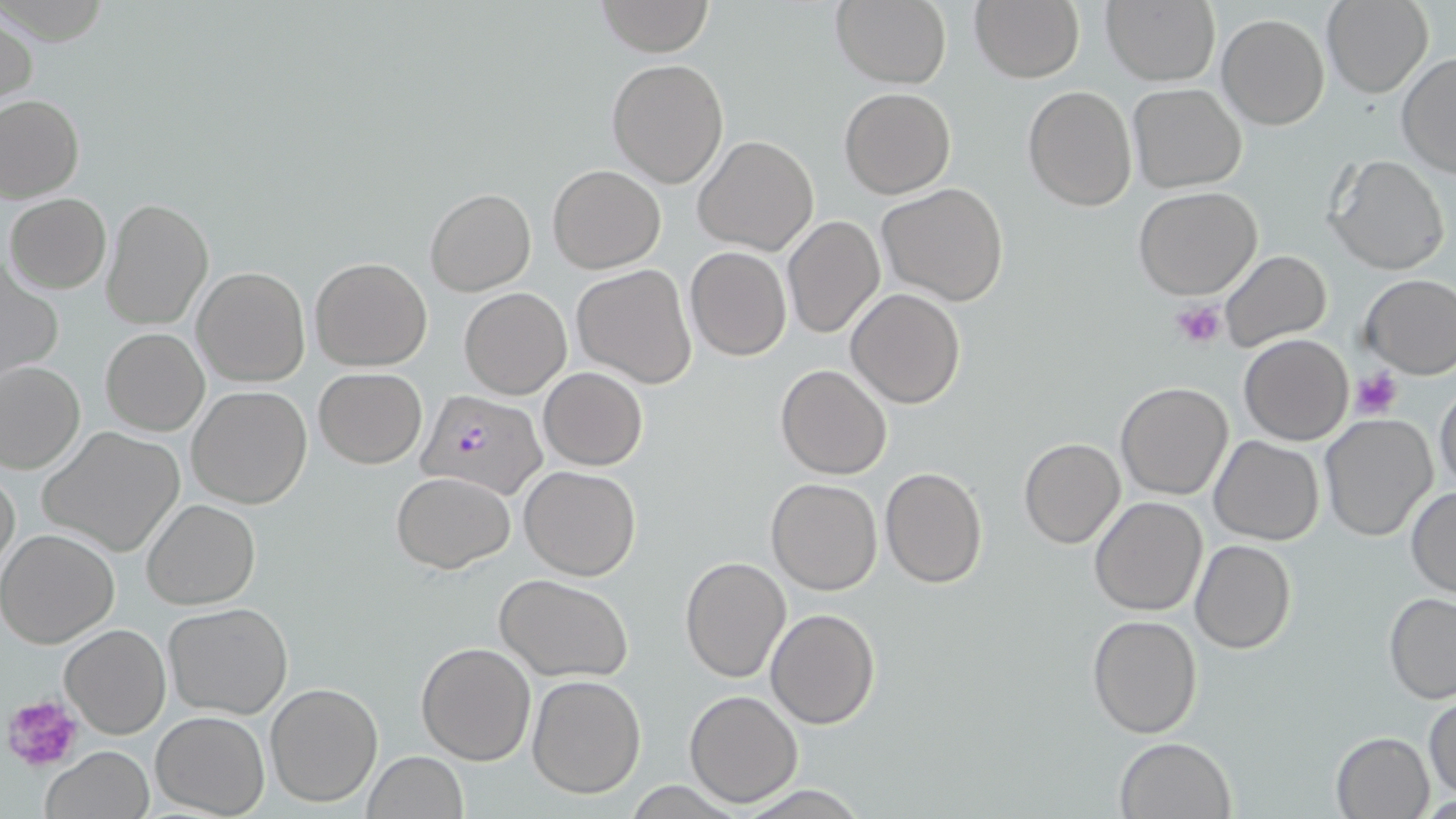

slide_level_diagnosis: Plasmodium falciparum
platelet_locations: 'approximate bounding boxes as [x1, y1, x2, y2] in pixels: [1172, 299, 1226, 351], [1349, 369, 1404, 420], [5, 694, 85, 770]'
stain: May-Grünwald-Giemsa
image_size: 1456×819 pixels
modality: light microscopy
preparation: thin blood smear
plasmodium_falciparum_infected_red_blood_cell_locations: 'approximate bounding boxes as [x1, y1, x2, y2] in pixels: [418, 390, 548, 501]'
field_of_view: one of a larger specimen
magnification: 1000x
uninfected_red_blood_cell_locations: 'approximate bounding boxes as [x1, y1, x2, y2] in pixels: [971, 0, 1085, 85], [1101, 0, 1219, 88], [596, 1, 714, 56], [830, 1, 951, 88], [1322, 1, 1432, 97], [1, 9, 37, 113], [1215, 13, 1329, 130], [1396, 53, 1456, 179], [605, 58, 729, 189], [1128, 84, 1247, 193], [1022, 85, 1137, 212], [839, 87, 956, 199], [0, 94, 84, 202], [693, 135, 820, 256], [1325, 153, 1450, 276], [548, 164, 665, 273], [876, 182, 1010, 306], [1132, 186, 1262, 300], [425, 189, 536, 296], [5, 193, 111, 294], [100, 198, 214, 331], [781, 215, 885, 339], [684, 247, 792, 362], [1218, 249, 1331, 352], [309, 256, 433, 370], [1, 261, 64, 383], [573, 264, 696, 389], [192, 265, 309, 387], [1360, 274, 1456, 379], [459, 286, 572, 399], [846, 288, 965, 409], [100, 327, 209, 436], [1239, 334, 1353, 446], [1, 361, 85, 473], [775, 365, 892, 480], [313, 367, 427, 468], [539, 367, 648, 471], [1434, 378, 1456, 496], [1115, 381, 1234, 500], [186, 385, 313, 510], [1318, 413, 1439, 543], [37, 425, 187, 557], [1210, 435, 1324, 544], [1018, 437, 1126, 549], [1, 461, 20, 579], [519, 465, 642, 581], [879, 466, 988, 587], [392, 471, 515, 573], [766, 477, 882, 596], [1405, 485, 1456, 598], [1088, 496, 1208, 616], [142, 499, 260, 610], [0, 528, 119, 648], [1190, 540, 1296, 655], [680, 557, 790, 682], [495, 574, 633, 681], [1383, 592, 1456, 704], [163, 601, 294, 718], [765, 608, 880, 731], [1087, 614, 1203, 738], [61, 623, 171, 738], [416, 641, 536, 766], [526, 674, 646, 799], [264, 681, 383, 807], [684, 689, 802, 806], [1424, 694, 1455, 801], [151, 710, 270, 818], [1330, 732, 1435, 818], [1114, 736, 1237, 819], [42, 747, 154, 819], [361, 751, 468, 819]'